Report the malaria status of this cell.
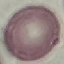
It is uninfected.

capture = smartphone through the microscope eyepiece
image type = cell patch, automatically extracted from a larger field of view and resized to 64 × 64 pixels
preparation = thin smear
stain = Giemsa